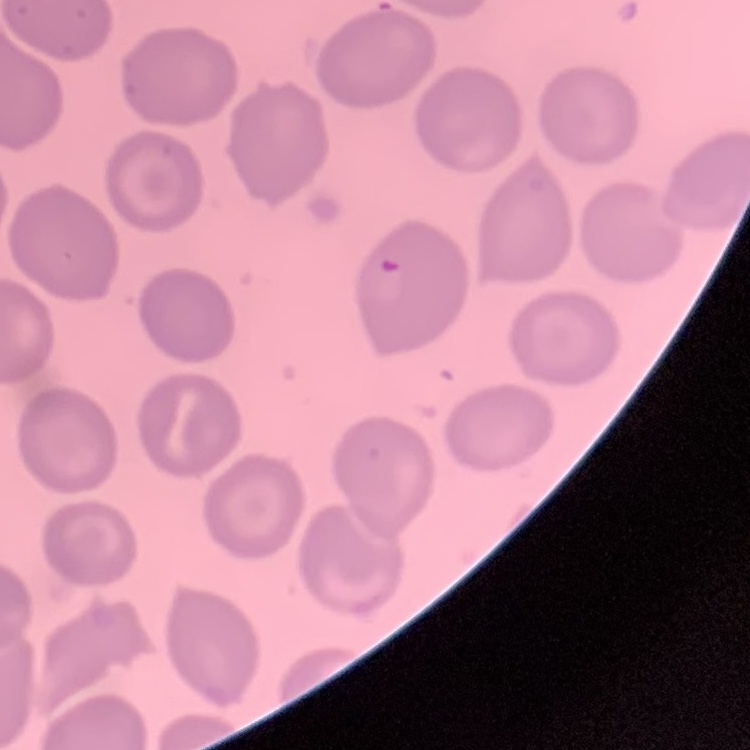

Summary:
  - Erythrocyte morphology: no rouleaux formation
  - Image type: one tile cut from a larger photomicrograph
  - Preparation: thin blood smear
  - Stain: Field's or Giemsa